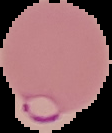

{
  "malaria_status": "parasitized",
  "preparation": "thin blood smear",
  "image_size": "112×133 pixels",
  "image_type": "cell region segmented out of the field of view; surrounding area masked to black"
}